Assess this cell for malaria.
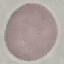

Uninfected.

image_type: cell patch, automatically extracted from a larger field of view and resized to 64 × 64 pixels
preparation: thin smear
stain: Giemsa
capture: smartphone through the microscope eyepiece